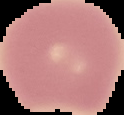
image type = segmented cell region with the area outside set to black
result = no Plasmodium parasites detected
preparation = thin blood smear
image size = 124×115 pixels